Comment on the morphology of the red blood cells.
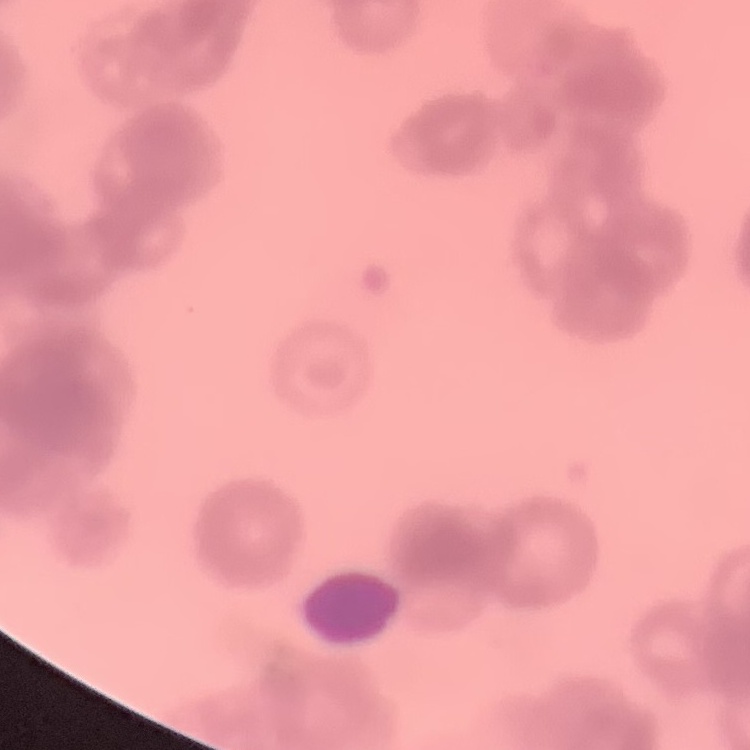
They show rouleaux formation.

Square crop of a larger photomicrograph. Thin peripheral smear. Stained with either Field's or Giemsa.